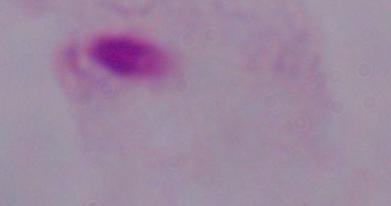

modality = micrograph
magnification = 1000x
identification = trichomonad